Outline each blood parasite and name the species.
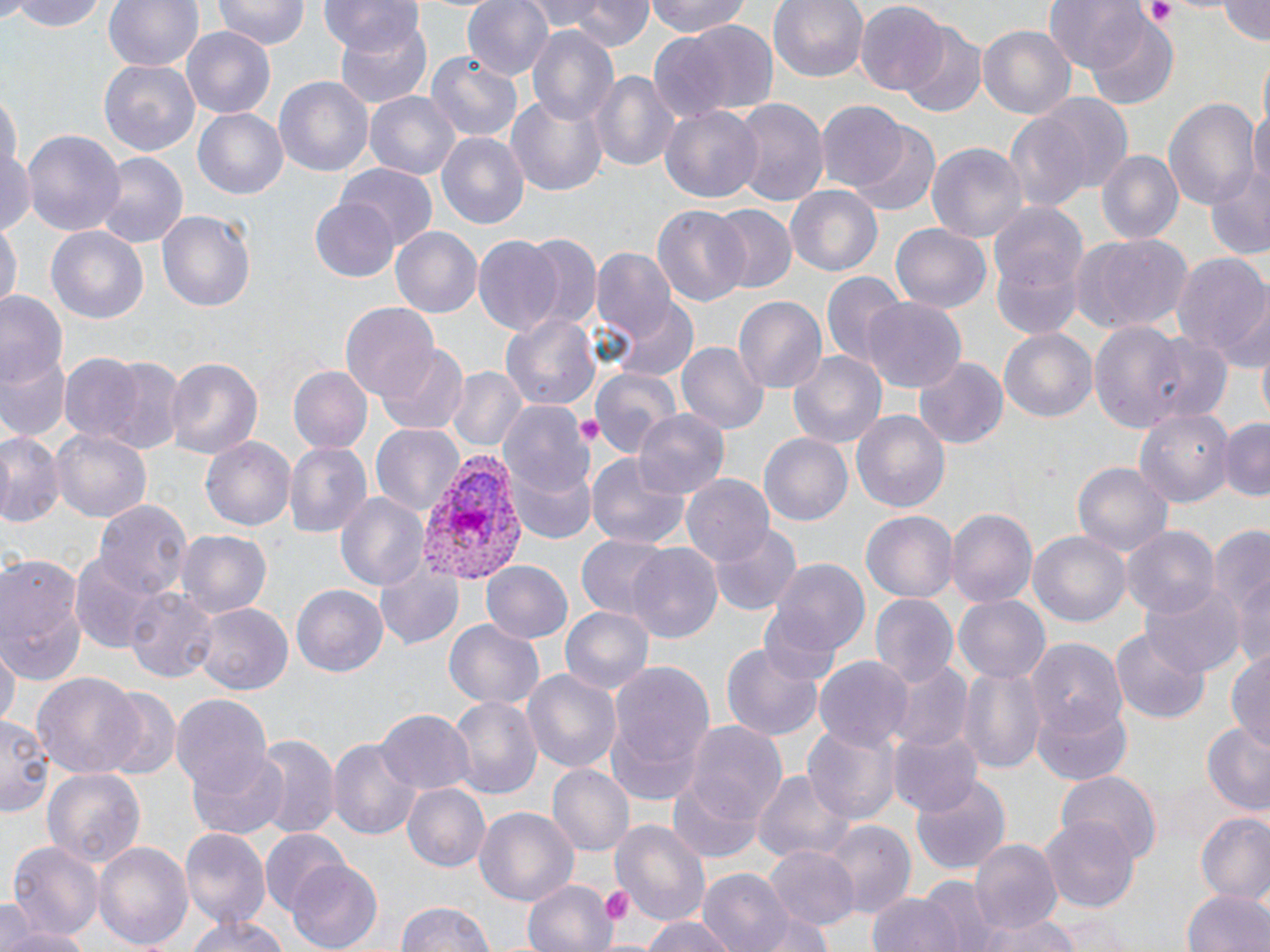
Approximate bounding boxes as named x1/y1/x2/y2 corners in pixels.
Plasmodium vivax-infected red blood cells: (x1=415, y1=453, x2=531, y2=587).
No Plasmodium falciparum, Plasmodium ovale, Plasmodium malariae, Babesia divergens, or Trypanosoma brucei observed.

slide-level diagnosis = Plasmodium vivax
preparation = thin blood film
image size = 1270×952 pixels
field of view = single
stain = May-Grünwald-Giemsa
magnification = 1000x
uninfected red blood cell locations = approximate bounding boxes as named x1/y1/x2/y2 corners in pixels: (x1=8, y1=0, x2=107, y2=31), (x1=103, y1=0, x2=204, y2=72), (x1=214, y1=0, x2=309, y2=52), (x1=320, y1=0, x2=424, y2=57), (x1=462, y1=0, x2=556, y2=82), (x1=561, y1=0, x2=651, y2=51), (x1=643, y1=0, x2=757, y2=39), (x1=769, y1=0, x2=868, y2=83), (x1=855, y1=0, x2=948, y2=95), (x1=1045, y1=0, x2=1147, y2=74), (x1=1216, y1=0, x2=1270, y2=44), (x1=330, y1=13, x2=433, y2=106), (x1=1087, y1=16, x2=1179, y2=107), (x1=666, y1=20, x2=782, y2=117), (x1=902, y1=25, x2=987, y2=117), (x1=978, y1=25, x2=1074, y2=117), (x1=181, y1=27, x2=277, y2=120), (x1=526, y1=27, x2=617, y2=124), (x1=646, y1=33, x2=735, y2=124), (x1=425, y1=50, x2=523, y2=144), (x1=100, y1=60, x2=199, y2=155), (x1=591, y1=68, x2=681, y2=175), (x1=275, y1=75, x2=373, y2=179), (x1=365, y1=91, x2=463, y2=181), (x1=1030, y1=93, x2=1133, y2=191), (x1=506, y1=96, x2=607, y2=195), (x1=1165, y1=96, x2=1261, y2=212), (x1=731, y1=97, x2=827, y2=207), (x1=815, y1=103, x2=909, y2=192), (x1=1251, y1=103, x2=1270, y2=194), (x1=659, y1=104, x2=764, y2=206), (x1=194, y1=108, x2=287, y2=200), (x1=1003, y1=116, x2=1090, y2=212), (x1=850, y1=123, x2=940, y2=217), (x1=22, y1=130, x2=125, y2=241), (x1=436, y1=132, x2=529, y2=231), (x1=927, y1=142, x2=1027, y2=242), (x1=0, y1=146, x2=34, y2=237), (x1=1094, y1=149, x2=1184, y2=247), (x1=94, y1=153, x2=187, y2=249), (x1=1206, y1=157, x2=1270, y2=259), (x1=336, y1=162, x2=438, y2=254), (x1=784, y1=187, x2=883, y2=278), (x1=311, y1=200, x2=397, y2=282), (x1=986, y1=202, x2=1089, y2=331), (x1=653, y1=204, x2=750, y2=307), (x1=710, y1=204, x2=797, y2=293), (x1=158, y1=209, x2=257, y2=314), (x1=0, y1=218, x2=19, y2=318), (x1=45, y1=225, x2=149, y2=324), (x1=892, y1=225, x2=990, y2=313), (x1=392, y1=227, x2=481, y2=317), (x1=521, y1=233, x2=604, y2=333), (x1=1069, y1=234, x2=1194, y2=334), (x1=471, y1=235, x2=564, y2=335), (x1=592, y1=247, x2=677, y2=345), (x1=1169, y1=253, x2=1270, y2=361), (x1=821, y1=271, x2=907, y2=366), (x1=1222, y1=291, x2=1270, y2=376), (x1=0, y1=292, x2=64, y2=390), (x1=733, y1=295, x2=826, y2=394), (x1=863, y1=298, x2=966, y2=394), (x1=611, y1=300, x2=699, y2=384), (x1=340, y1=301, x2=440, y2=400), (x1=501, y1=311, x2=600, y2=415), (x1=1088, y1=321, x2=1190, y2=435), (x1=998, y1=326, x2=1100, y2=423), (x1=1133, y1=332, x2=1237, y2=427), (x1=677, y1=341, x2=767, y2=435), (x1=2, y1=343, x2=70, y2=444), (x1=376, y1=345, x2=467, y2=434), (x1=787, y1=351, x2=887, y2=449), (x1=58, y1=352, x2=145, y2=444), (x1=90, y1=354, x2=188, y2=456), (x1=165, y1=356, x2=264, y2=460), (x1=915, y1=358, x2=1006, y2=449), (x1=446, y1=366, x2=526, y2=452), (x1=287, y1=367, x2=370, y2=453), (x1=590, y1=367, x2=682, y2=460), (x1=500, y1=400, x2=594, y2=501), (x1=1136, y1=408, x2=1235, y2=510), (x1=634, y1=409, x2=729, y2=501), (x1=852, y1=410, x2=949, y2=512), (x1=1218, y1=416, x2=1270, y2=500), (x1=371, y1=424, x2=465, y2=514), (x1=52, y1=427, x2=151, y2=523), (x1=0, y1=429, x2=62, y2=526), (x1=760, y1=434, x2=852, y2=525), (x1=201, y1=437, x2=296, y2=533), (x1=283, y1=441, x2=370, y2=538), (x1=587, y1=453, x2=692, y2=550), (x1=508, y1=461, x2=596, y2=547), (x1=1072, y1=462, x2=1173, y2=556), (x1=682, y1=474, x2=772, y2=567), (x1=335, y1=491, x2=431, y2=592), (x1=93, y1=499, x2=190, y2=599), (x1=945, y1=509, x2=1036, y2=609), (x1=862, y1=511, x2=956, y2=601), (x1=1212, y1=521, x2=1269, y2=669), (x1=1121, y1=523, x2=1220, y2=620), (x1=708, y1=525, x2=800, y2=615), (x1=175, y1=530, x2=272, y2=617), (x1=1030, y1=530, x2=1133, y2=628), (x1=577, y1=535, x2=674, y2=621), (x1=626, y1=545, x2=722, y2=645), (x1=71, y1=553, x2=165, y2=650), (x1=0, y1=554, x2=87, y2=682), (x1=373, y1=555, x2=465, y2=651), (x1=767, y1=559, x2=871, y2=665), (x1=483, y1=561, x2=571, y2=642), (x1=1140, y1=580, x2=1244, y2=677), (x1=293, y1=585, x2=387, y2=677), (x1=125, y1=587, x2=215, y2=683), (x1=869, y1=594, x2=958, y2=689), (x1=955, y1=595, x2=1048, y2=682), (x1=197, y1=603, x2=292, y2=696), (x1=560, y1=604, x2=655, y2=694), (x1=443, y1=619, x2=544, y2=712), (x1=1110, y1=630, x2=1210, y2=724), (x1=722, y1=638, x2=826, y2=744), (x1=1025, y1=642, x2=1128, y2=741), (x1=1, y1=645, x2=17, y2=735), (x1=1227, y1=651, x2=1270, y2=748), (x1=815, y1=657, x2=913, y2=753), (x1=887, y1=663, x2=972, y2=754), (x1=607, y1=664, x2=716, y2=787), (x1=959, y1=665, x2=1045, y2=772), (x1=521, y1=667, x2=622, y2=775), (x1=29, y1=672, x2=146, y2=783), (x1=99, y1=688, x2=179, y2=780), (x1=171, y1=693, x2=273, y2=793), (x1=1032, y1=695, x2=1133, y2=784), (x1=449, y1=697, x2=542, y2=799), (x1=377, y1=708, x2=474, y2=794), (x1=0, y1=715, x2=52, y2=815), (x1=685, y1=721, x2=787, y2=832), (x1=804, y1=723, x2=898, y2=827), (x1=1201, y1=725, x2=1270, y2=815), (x1=890, y1=731, x2=983, y2=816), (x1=255, y1=735, x2=339, y2=842), (x1=328, y1=736, x2=422, y2=843), (x1=186, y1=752, x2=289, y2=840), (x1=41, y1=765, x2=146, y2=869), (x1=548, y1=765, x2=632, y2=854), (x1=754, y1=767, x2=855, y2=866), (x1=1055, y1=770, x2=1162, y2=864), (x1=909, y1=775, x2=1010, y2=878), (x1=668, y1=776, x2=764, y2=864), (x1=402, y1=783, x2=490, y2=872), (x1=474, y1=806, x2=579, y2=904), (x1=1193, y1=812, x2=1270, y2=902), (x1=1042, y1=815, x2=1138, y2=914), (x1=612, y1=819, x2=711, y2=926), (x1=823, y1=822, x2=915, y2=916), (x1=181, y1=830, x2=268, y2=929), (x1=262, y1=830, x2=355, y2=917), (x1=971, y1=837, x2=1061, y2=934), (x1=8, y1=839, x2=103, y2=942), (x1=95, y1=841, x2=192, y2=950), (x1=767, y1=847, x2=856, y2=932), (x1=286, y1=861, x2=384, y2=950), (x1=699, y1=867, x2=795, y2=952), (x1=522, y1=877, x2=615, y2=952), (x1=922, y1=877, x2=1002, y2=952), (x1=1182, y1=888, x2=1270, y2=952), (x1=867, y1=894, x2=962, y2=952), (x1=0, y1=900, x2=32, y2=952), (x1=394, y1=901, x2=497, y2=952), (x1=748, y1=904, x2=838, y2=952), (x1=984, y1=912, x2=1076, y2=952), (x1=185, y1=914, x2=286, y2=952), (x1=639, y1=915, x2=741, y2=952), (x1=2, y1=924, x2=92, y2=952)
modality = light microscopy
platelet locations = approximate bounding boxes as named x1/y1/x2/y2 corners in pixels: (x1=1140, y1=1, x2=1178, y2=27), (x1=574, y1=414, x2=608, y2=448), (x1=599, y1=885, x2=635, y2=925)